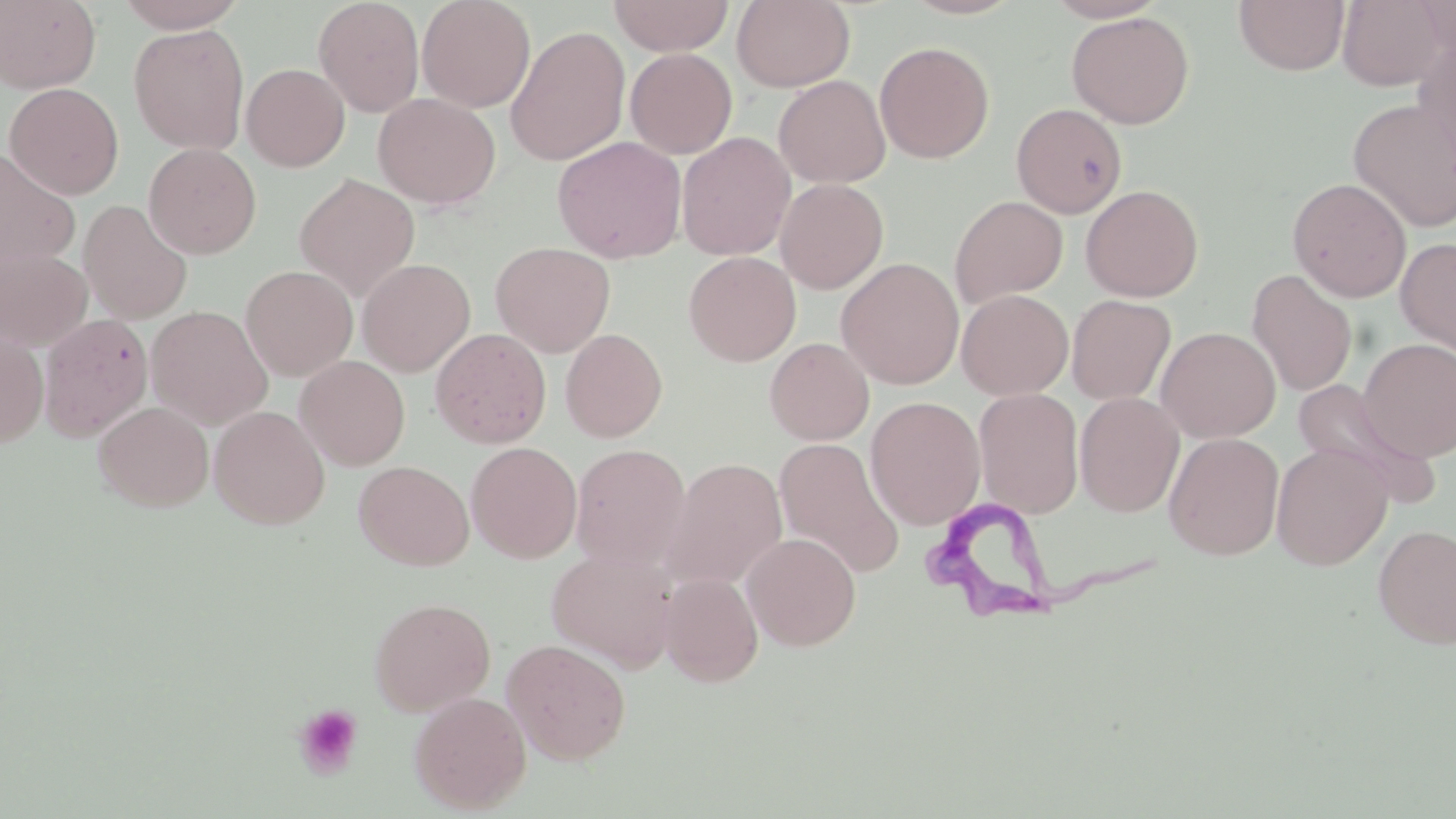 Approximate bounding boxes as (x1,y1)-(x2,y2) corner pairs in pixels. Platelet locations: (293,703)-(363,778). Trypanosoma brucei locations: (924,499)-(1160,620). Uninfected red blood cell locations: (113,0)-(250,32), (313,0)-(425,117), (417,0)-(536,113), (609,0)-(735,56), (732,0)-(855,91), (900,0)-(1025,20), (1044,0)-(1168,23), (1233,0)-(1350,76), (1336,0)-(1453,91), (1415,0)-(1456,61), (0,1)-(101,93), (1066,11)-(1194,129), (128,24)-(250,155), (505,25)-(631,166), (1413,35)-(1456,171), (874,41)-(995,164), (625,48)-(738,159), (241,63)-(350,172), (773,75)-(891,189), (4,82)-(124,200), (373,92)-(500,210), (1349,98)-(1456,232), (1011,102)-(1128,217), (676,132)-(796,261), (552,136)-(687,263), (143,142)-(261,259), (0,147)-(80,275), (294,173)-(420,301), (1287,177)-(1412,302), (775,178)-(889,294), (1080,184)-(1204,302), (949,195)-(1068,307), (78,200)-(193,324), (1395,237)-(1456,361), (490,241)-(615,357), (0,247)-(93,352), (683,251)-(801,366), (357,258)-(475,376), (836,258)-(964,389), (240,265)-(358,381), (1246,269)-(1357,396), (956,289)-(1074,400), (1067,294)-(1176,405), (146,306)-(273,430), (38,313)-(152,442), (1156,326)-(1280,443), (0,327)-(49,448), (430,327)-(551,449), (560,328)-(667,443), (564,330)-(674,566), (764,337)-(874,445), (1358,337)-(1456,462), (295,355)-(410,470), (1289,377)-(1435,501), (973,387)-(1084,519), (1074,392)-(1184,517), (865,396)-(986,530), (92,400)-(214,511), (209,405)-(330,529), (1163,432)-(1285,561), (773,436)-(904,577), (466,442)-(582,563), (570,443)-(692,571), (1271,443)-(1393,570), (662,457)-(788,591), (353,460)-(474,570), (1373,524)-(1456,650), (741,532)-(862,651), (546,547)-(679,672), (659,573)-(763,687), (369,596)-(496,716), (502,639)-(631,764), (408,691)-(531,813). Slide-level diagnosis: Trypanosoma brucei. Captured at 1000x magnification. May-Grünwald-Giemsa stain. Image is 1456×819 pixels. Optical microscopy. Single field of view. Thin blood smear.